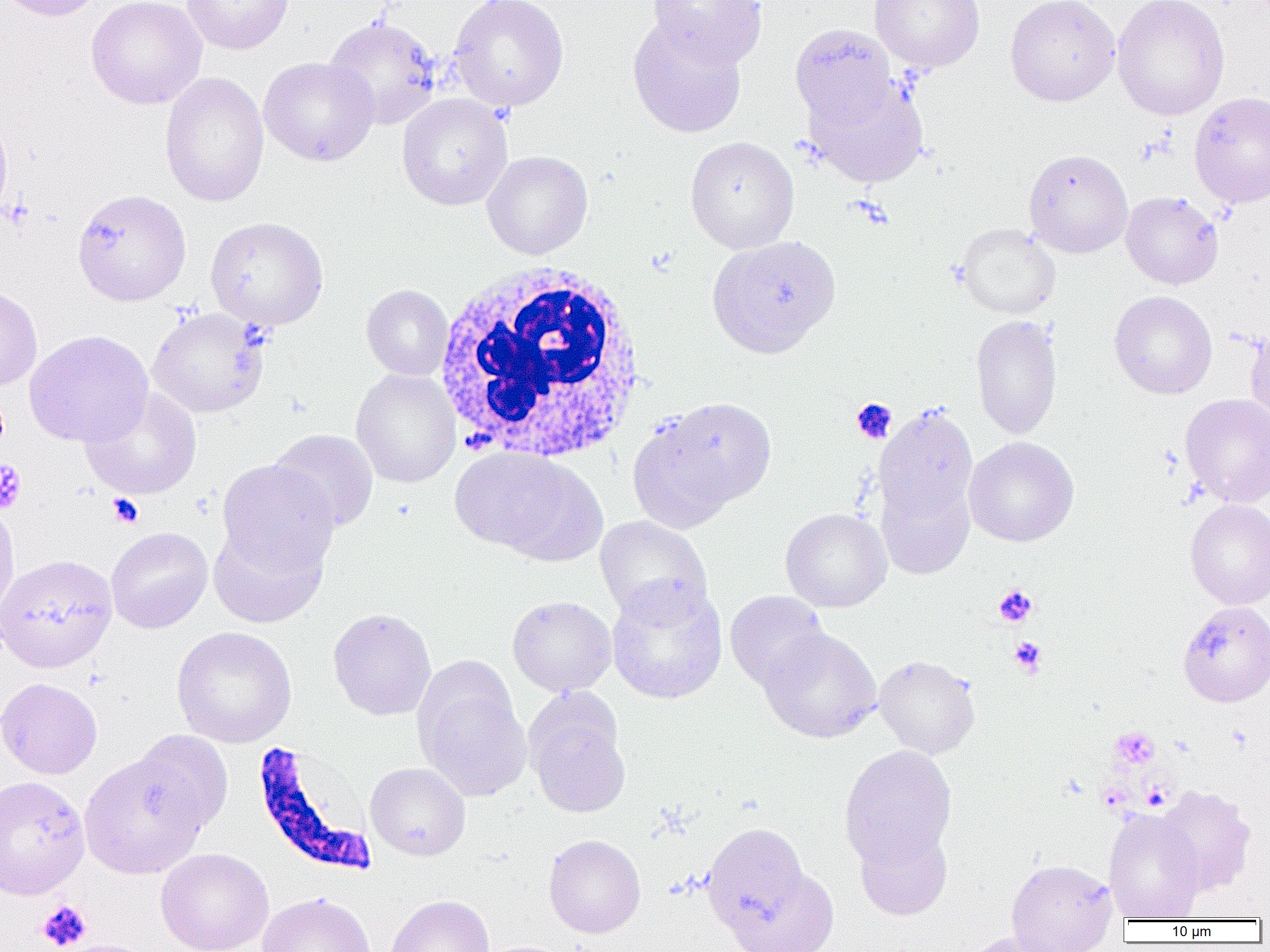
Summary:
  - Coordinate format: approximate bounding boxes as [x1, y1, x2, y2] in pixels
  - Platelet locations: [1, 197, 35, 230], [851, 398, 897, 443], [0, 459, 27, 515], [108, 493, 144, 528], [993, 584, 1037, 627], [1009, 637, 1046, 675], [1111, 727, 1159, 769], [1097, 783, 1131, 811], [36, 900, 92, 951]
  - Uninfected red blood cell locations: [0, 0, 108, 22], [85, 0, 207, 109], [182, 0, 295, 55], [448, 0, 570, 112], [648, 0, 767, 67], [869, 0, 985, 72], [1004, 0, 1120, 106], [1112, 0, 1230, 120], [323, 15, 443, 130], [627, 16, 747, 138], [789, 24, 896, 129], [258, 56, 378, 166], [159, 71, 269, 207], [806, 76, 929, 187], [1189, 91, 1270, 209], [397, 93, 513, 211], [0, 108, 12, 223], [685, 136, 799, 254], [1023, 148, 1133, 258], [482, 151, 593, 259], [72, 188, 192, 307], [1121, 191, 1223, 289], [205, 216, 329, 330], [956, 223, 1061, 319], [707, 235, 841, 358], [361, 284, 453, 381], [0, 286, 43, 391], [1109, 290, 1217, 399], [147, 306, 269, 418], [971, 314, 1062, 440], [1245, 326, 1270, 424], [24, 330, 154, 447], [351, 369, 460, 488], [80, 388, 202, 500], [1180, 393, 1270, 507], [633, 396, 777, 524], [874, 404, 979, 531], [268, 428, 379, 534], [964, 436, 1079, 547], [450, 447, 590, 559], [215, 459, 339, 580], [876, 473, 975, 580], [1185, 498, 1270, 609], [0, 503, 20, 620], [781, 507, 891, 612], [595, 515, 713, 623], [208, 520, 330, 628], [106, 526, 213, 634], [0, 553, 118, 673], [606, 580, 728, 705], [725, 590, 830, 694], [507, 595, 617, 696], [1177, 602, 1270, 707], [328, 608, 437, 721], [171, 626, 297, 748], [758, 627, 882, 743], [874, 655, 980, 759], [413, 667, 532, 801], [0, 678, 102, 779], [524, 694, 631, 818], [130, 730, 233, 837], [839, 745, 957, 868], [79, 750, 210, 879], [365, 762, 470, 861], [0, 775, 90, 899], [1154, 785, 1256, 896], [1102, 809, 1205, 921], [702, 822, 809, 933], [855, 825, 953, 920], [543, 834, 646, 938], [155, 847, 274, 952], [1006, 858, 1118, 952], [726, 867, 840, 952], [256, 892, 375, 952], [385, 894, 495, 952], [962, 931, 1073, 952], [51, 938, 159, 952]
  - Plasmodium falciparum-infected red blood cell locations: [257, 743, 380, 874]
  - White blood cell locations: [431, 260, 648, 463]
  - Slide-level diagnosis: Plasmodium falciparum
  - Image size: 1270×952 pixels
  - Preparation: thin blood smear
  - Magnification: 1000x
  - Modality: light microscopy
  - Field of view: single